Assess this cell for malaria.
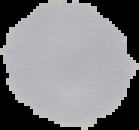
Uninfected.

Segmented cell region on a black background. From a thin blood smear. Image is 139×130 pixels.